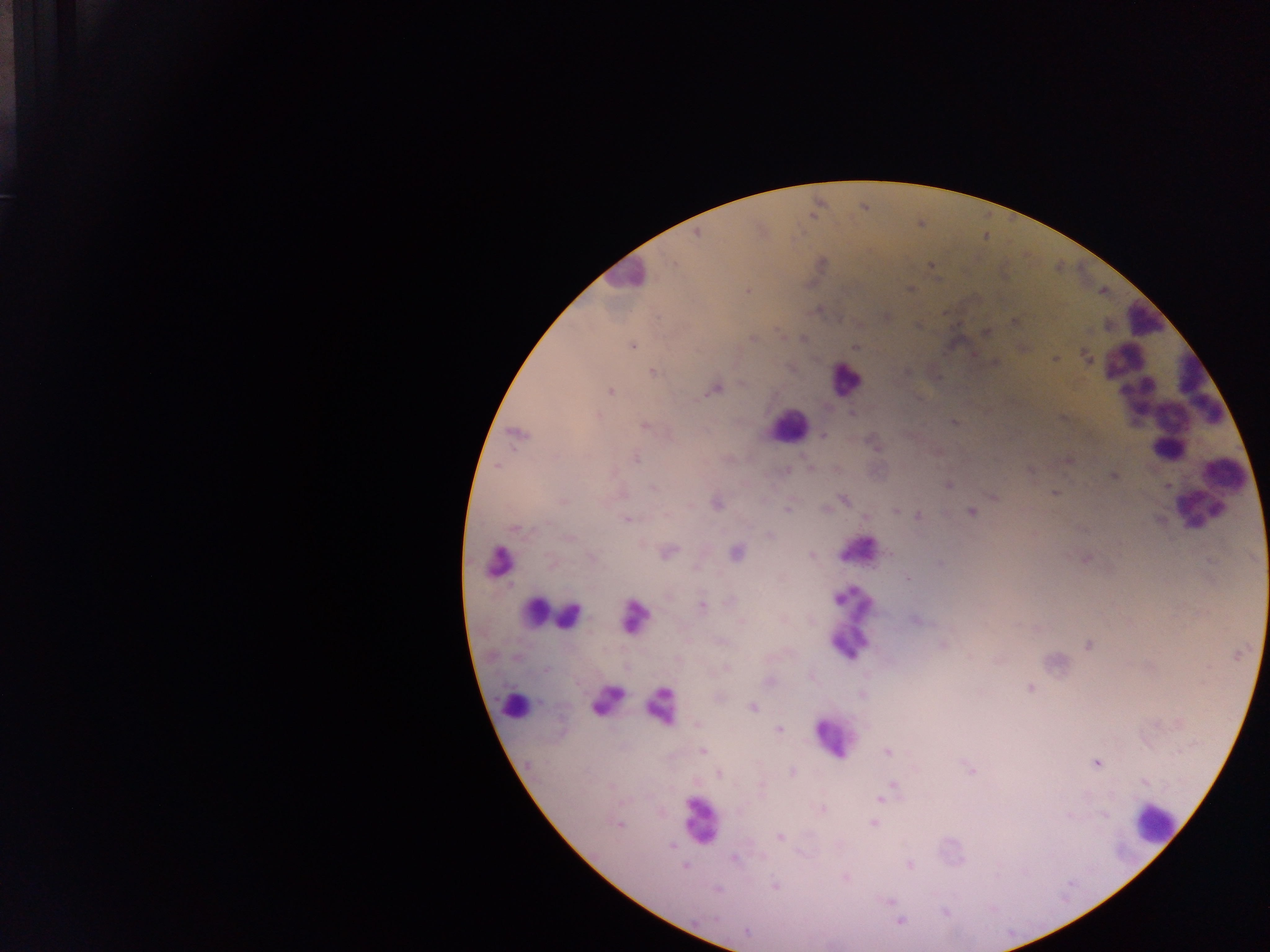
capture = mobile-phone photograph through a microscope
leukocyte locations = approximate centers as {x, y} in pixels: {622, 275}, {1144, 322}, {844, 379}, {1166, 406}, {788, 426}, {1225, 468}, {1197, 508}, {854, 544}, {501, 560}, {533, 610}, {561, 617}, {629, 617}, {849, 627}, {607, 697}, {657, 704}, {514, 705}, {832, 737}, {700, 822}, {1153, 824}
image size = 1270×952 pixels
malaria parasite locations = approximate centers as {x, y} in pixels: {696, 233}, {673, 263}, {931, 265}, {909, 289}, {747, 291}, {819, 310}, {886, 316}, {1014, 321}, {986, 331}, {752, 339}, {632, 346}, {855, 348}, {1086, 357}, {1055, 359}, {652, 372}, {907, 372}, {715, 389}, {610, 391}, {852, 413}, {598, 416}, {954, 422}, {645, 427}, {517, 434}, {823, 435}, {874, 444}, {635, 459}, {1068, 460}, {810, 468}, {786, 469}, {1029, 470}, {1113, 476}, {948, 485}, {653, 488}, {1055, 494}, {994, 497}, {563, 500}, {844, 500}, {717, 504}, {787, 509}, {896, 510}, {971, 512}, {918, 515}, {627, 517}, {865, 517}, {516, 530}, {770, 535}, {569, 538}, {669, 552}, {735, 552}, {811, 555}, {592, 557}, {1087, 559}, {549, 560}, {940, 564}, {906, 578}, {730, 601}, {702, 605}, {742, 620}, {916, 620}, {721, 642}, {942, 645}, {1088, 645}, {727, 669}, {545, 670}, {769, 681}, {1030, 688}, {752, 707}, {698, 724}, {779, 730}, {702, 751}, {887, 752}, {1097, 764}, {970, 769}, {792, 772}, {719, 775}, {893, 785}, {880, 799}, {822, 808}, {1104, 816}, {873, 824}, {618, 825}, {781, 837}, {671, 846}, {734, 858}, {909, 865}, {684, 866}, {846, 878}, {775, 887}, {716, 890}, {889, 902}, {944, 912}, {900, 922}, {746, 931}
country = Ghana
field of view = single
preparation = thick blood smear